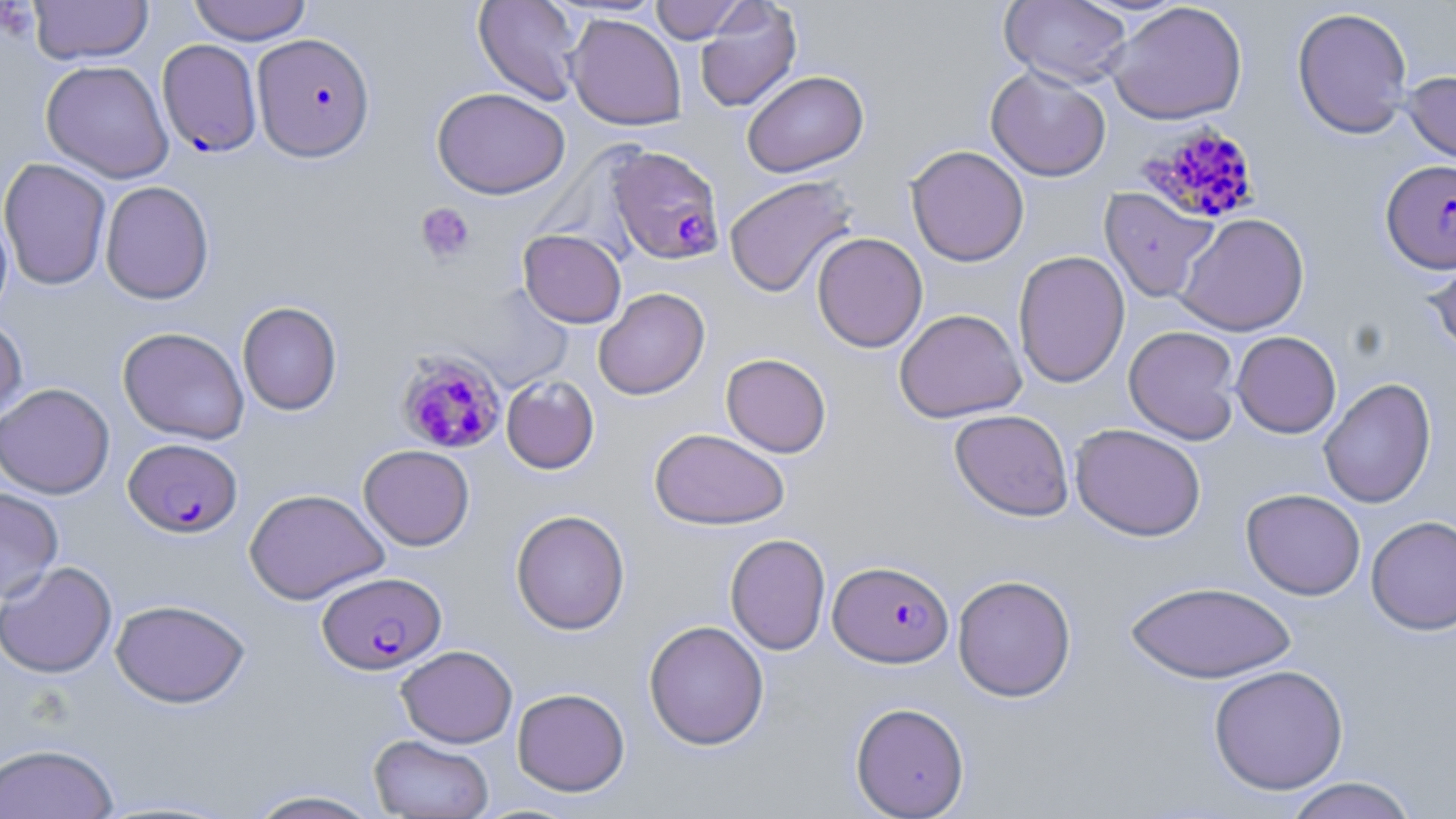
Summary:
  - Coordinate format: approximate bounding boxes as (x1,y1)-(x2,y2) corner pairs in pixels
  - Platelet locations: (416,202)-(476,263)
  - Plasmodium falciparum-infected red blood cell locations: (252,33)-(376,161), (157,39)-(263,157), (1138,122)-(1262,225), (607,145)-(726,265), (1381,159)-(1456,273), (395,349)-(507,455), (123,437)-(243,538), (828,560)-(954,668), (317,571)-(446,674)
  - Uninfected red blood cell locations: (188,0)-(312,45), (473,0)-(584,106), (650,0)-(749,43), (999,0)-(1132,88), (29,1)-(153,65), (694,1)-(802,113), (1106,2)-(1248,124), (1292,7)-(1414,139), (565,14)-(687,130), (40,60)-(174,183), (985,66)-(1112,181), (742,70)-(869,177), (1401,70)-(1456,168), (432,87)-(570,199), (905,145)-(1030,267), (0,157)-(112,291), (724,175)-(859,297), (99,181)-(214,304), (1099,187)-(1218,303), (0,205)-(13,324), (1176,213)-(1310,336), (518,229)-(626,328), (811,232)-(928,352), (1423,241)-(1456,359), (1013,251)-(1130,388), (594,287)-(709,400), (237,301)-(342,416), (894,309)-(1026,423), (0,316)-(28,427), (118,326)-(249,444), (1124,326)-(1241,444), (1231,331)-(1341,438), (721,353)-(832,458), (501,375)-(600,474), (1318,377)-(1436,509), (0,382)-(115,499), (949,409)-(1074,520), (1070,423)-(1206,541), (649,427)-(790,529), (358,444)-(475,550), (0,486)-(64,602), (243,488)-(389,605), (1241,488)-(1366,600), (511,509)-(630,635), (1366,515)-(1456,636), (725,533)-(830,656), (0,561)-(117,678), (952,574)-(1076,701), (1125,580)-(1297,683), (110,599)-(249,708), (643,620)-(769,750), (396,645)-(518,748), (1208,664)-(1349,795), (512,687)-(630,796), (850,701)-(969,818), (368,734)-(494,818), (0,743)-(119,818), (1282,776)-(1420,819), (243,788)-(384,818)
  - Slide-level diagnosis: Plasmodium falciparum
  - Stain: May-Grünwald-Giemsa
  - Field of view: one of a larger specimen
  - Magnification: 1000x
  - Modality: light microscopy
  - Image size: 1456×819 pixels
  - Preparation: thin blood smear